Outline each uninfected red blood cell.
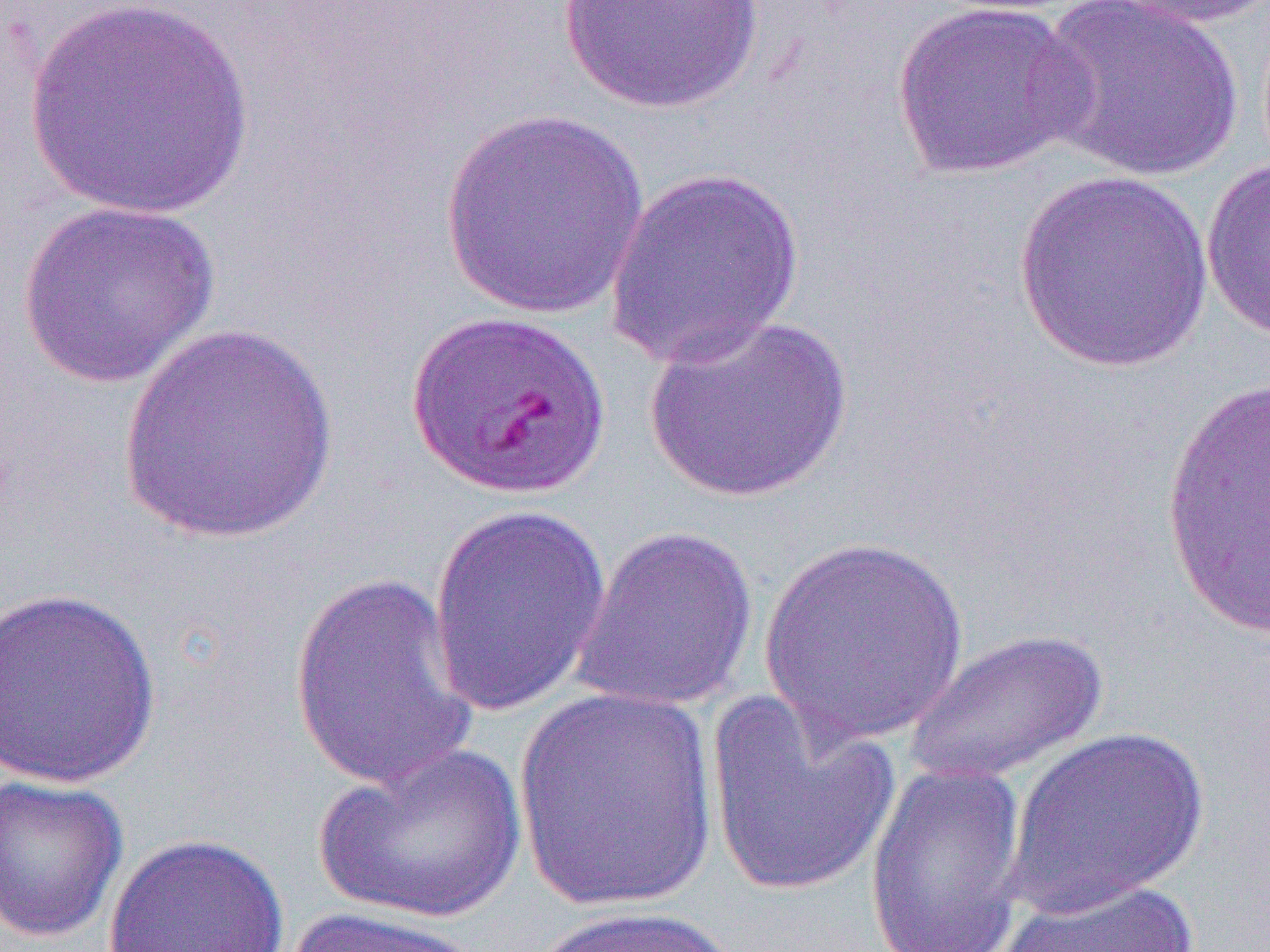
Approximate bounding boxes as named x1/y1/x2/y2 corners in pixels.
Uninfected red blood cells: (x1=24, y1=0, x2=254, y2=221), (x1=554, y1=0, x2=770, y2=115), (x1=1032, y1=0, x2=1244, y2=184), (x1=1101, y1=0, x2=1269, y2=30), (x1=891, y1=1, x2=1092, y2=180), (x1=438, y1=107, x2=653, y2=321), (x1=1201, y1=157, x2=1270, y2=342), (x1=604, y1=166, x2=807, y2=370), (x1=1012, y1=170, x2=1217, y2=373), (x1=16, y1=199, x2=220, y2=390), (x1=644, y1=312, x2=852, y2=502), (x1=116, y1=320, x2=341, y2=546), (x1=1159, y1=371, x2=1269, y2=640), (x1=426, y1=504, x2=613, y2=718), (x1=570, y1=523, x2=760, y2=712), (x1=756, y1=535, x2=972, y2=750), (x1=287, y1=568, x2=484, y2=796), (x1=0, y1=586, x2=163, y2=790), (x1=904, y1=627, x2=1110, y2=787), (x1=513, y1=685, x2=721, y2=914), (x1=703, y1=693, x2=901, y2=900), (x1=1004, y1=725, x2=1210, y2=916), (x1=313, y1=740, x2=529, y2=925), (x1=864, y1=761, x2=1030, y2=951), (x1=0, y1=774, x2=129, y2=943), (x1=102, y1=832, x2=291, y2=952), (x1=987, y1=877, x2=1202, y2=952), (x1=529, y1=903, x2=742, y2=952), (x1=282, y1=906, x2=487, y2=952).

Slide-level diagnosis: Plasmodium falciparum. Optical microscopy. Captured at 1000x magnification. Thin blood smear. Single field of view. Image is 1270×952 pixels.